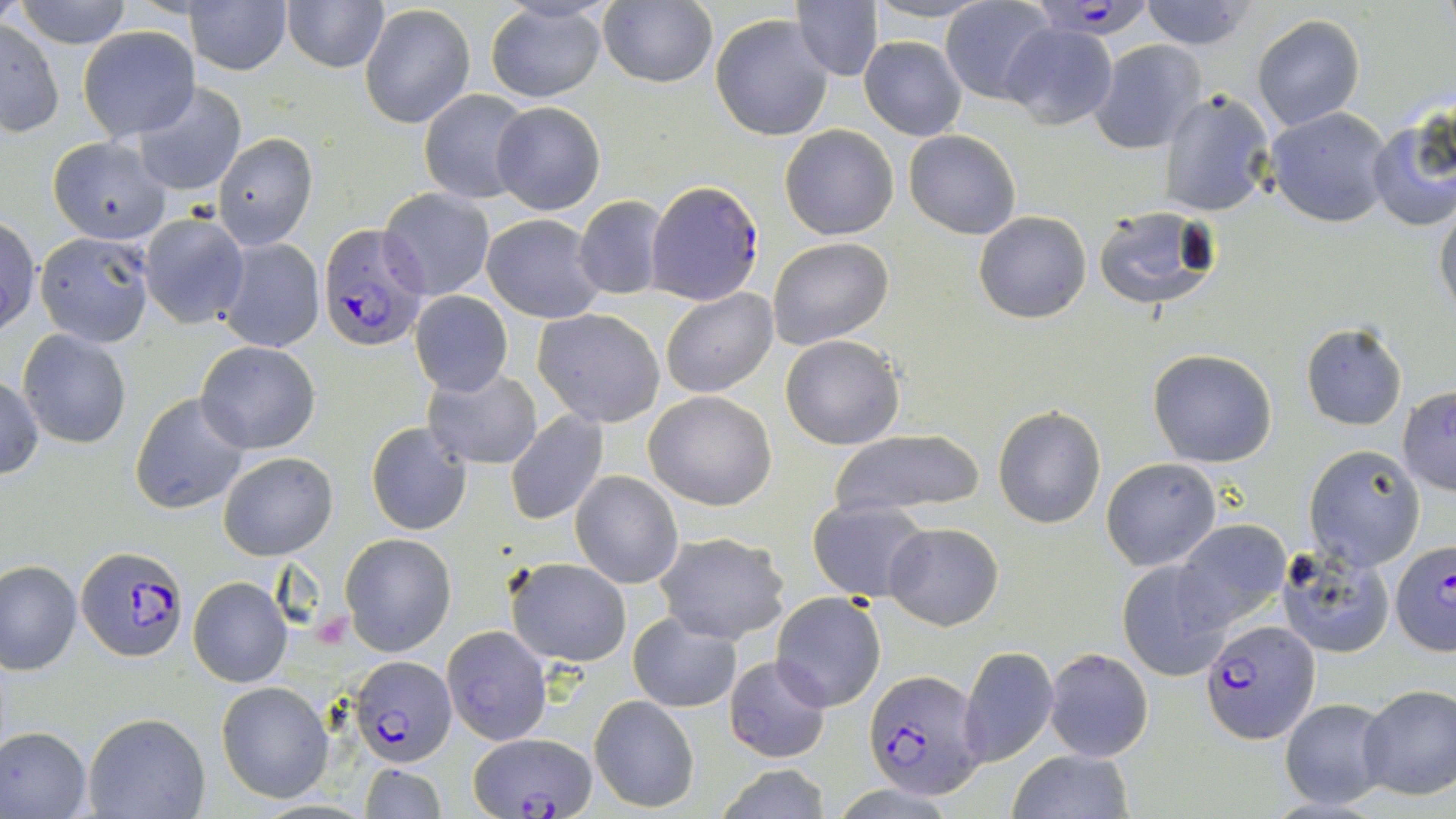

Summary:
  - Coordinate format: approximate bounding boxes as named x1/y1/x2/y2 corners in pixels
  - Plasmodium falciparum-infected red blood cell locations: (x1=1042, y1=0, x2=1148, y2=42), (x1=649, y1=181, x2=762, y2=304), (x1=318, y1=223, x2=431, y2=353), (x1=1388, y1=541, x2=1456, y2=658), (x1=76, y1=546, x2=186, y2=660), (x1=1202, y1=621, x2=1318, y2=743), (x1=353, y1=655, x2=457, y2=768), (x1=864, y1=670, x2=988, y2=798), (x1=470, y1=732, x2=596, y2=819)
  - Uninfected red blood cell locations: (x1=0, y1=0, x2=26, y2=31), (x1=15, y1=0, x2=132, y2=48), (x1=186, y1=0, x2=293, y2=75), (x1=601, y1=0, x2=717, y2=88), (x1=793, y1=0, x2=884, y2=82), (x1=941, y1=0, x2=1057, y2=104), (x1=1141, y1=0, x2=1254, y2=49), (x1=283, y1=1, x2=389, y2=73), (x1=866, y1=1, x2=987, y2=27), (x1=359, y1=3, x2=476, y2=129), (x1=485, y1=3, x2=609, y2=103), (x1=710, y1=14, x2=834, y2=141), (x1=1251, y1=15, x2=1365, y2=132), (x1=0, y1=19, x2=64, y2=135), (x1=1002, y1=23, x2=1117, y2=129), (x1=78, y1=27, x2=198, y2=140), (x1=860, y1=35, x2=967, y2=140), (x1=1089, y1=39, x2=1206, y2=153), (x1=132, y1=83, x2=247, y2=196), (x1=420, y1=88, x2=533, y2=205), (x1=1159, y1=89, x2=1276, y2=217), (x1=492, y1=101, x2=606, y2=215), (x1=1267, y1=105, x2=1396, y2=228), (x1=1365, y1=114, x2=1455, y2=233), (x1=780, y1=125, x2=899, y2=241), (x1=903, y1=130, x2=1021, y2=238), (x1=214, y1=133, x2=317, y2=249), (x1=49, y1=136, x2=171, y2=244), (x1=379, y1=188, x2=495, y2=301), (x1=574, y1=196, x2=669, y2=302), (x1=1434, y1=204, x2=1456, y2=323), (x1=1093, y1=205, x2=1222, y2=312), (x1=975, y1=211, x2=1091, y2=324), (x1=139, y1=212, x2=249, y2=328), (x1=482, y1=212, x2=606, y2=323), (x1=0, y1=216, x2=40, y2=335), (x1=35, y1=230, x2=157, y2=347), (x1=216, y1=236, x2=325, y2=353), (x1=767, y1=237, x2=893, y2=351), (x1=660, y1=288, x2=778, y2=397), (x1=410, y1=291, x2=512, y2=396), (x1=534, y1=308, x2=665, y2=427), (x1=1300, y1=322, x2=1408, y2=431), (x1=17, y1=329, x2=132, y2=449), (x1=779, y1=334, x2=905, y2=451), (x1=196, y1=340, x2=320, y2=453), (x1=1148, y1=349, x2=1277, y2=466), (x1=422, y1=366, x2=542, y2=471), (x1=0, y1=374, x2=44, y2=480), (x1=1397, y1=386, x2=1456, y2=495), (x1=646, y1=390, x2=777, y2=511), (x1=130, y1=391, x2=250, y2=516), (x1=992, y1=405, x2=1107, y2=529), (x1=505, y1=410, x2=610, y2=524), (x1=366, y1=421, x2=472, y2=535), (x1=828, y1=428, x2=984, y2=521), (x1=1304, y1=445, x2=1427, y2=571), (x1=218, y1=452, x2=337, y2=559), (x1=1100, y1=458, x2=1221, y2=571), (x1=571, y1=471, x2=681, y2=588), (x1=808, y1=498, x2=928, y2=602), (x1=1171, y1=519, x2=1290, y2=631), (x1=882, y1=521, x2=1003, y2=630), (x1=653, y1=530, x2=790, y2=644), (x1=340, y1=534, x2=456, y2=657), (x1=1275, y1=542, x2=1396, y2=658), (x1=505, y1=557, x2=632, y2=668), (x1=1116, y1=558, x2=1237, y2=681), (x1=1, y1=560, x2=81, y2=674), (x1=188, y1=577, x2=292, y2=687), (x1=771, y1=593, x2=885, y2=713), (x1=628, y1=612, x2=742, y2=713), (x1=441, y1=626, x2=552, y2=745), (x1=959, y1=646, x2=1058, y2=766), (x1=1042, y1=647, x2=1154, y2=761), (x1=724, y1=655, x2=833, y2=763), (x1=216, y1=681, x2=333, y2=804), (x1=1358, y1=684, x2=1456, y2=800), (x1=589, y1=695, x2=700, y2=813), (x1=1278, y1=698, x2=1392, y2=810), (x1=83, y1=712, x2=209, y2=819), (x1=0, y1=727, x2=92, y2=818), (x1=1007, y1=748, x2=1134, y2=819), (x1=359, y1=761, x2=447, y2=819), (x1=712, y1=764, x2=834, y2=819)
  - Slide-level diagnosis: Plasmodium falciparum
  - Preparation: thin blood smear
  - Field of view: one of a larger specimen
  - Magnification: 1000x
  - Stain: May-Grünwald-Giemsa
  - Modality: optical microscopy
  - Image size: 1456×819 pixels